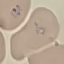

result = malaria parasites identified
stain = Giemsa
image type = automatically extracted cell patch, resized to 64 × 64 pixels
preparation = thin blood film
capture = smartphone camera at the microscope eyepiece